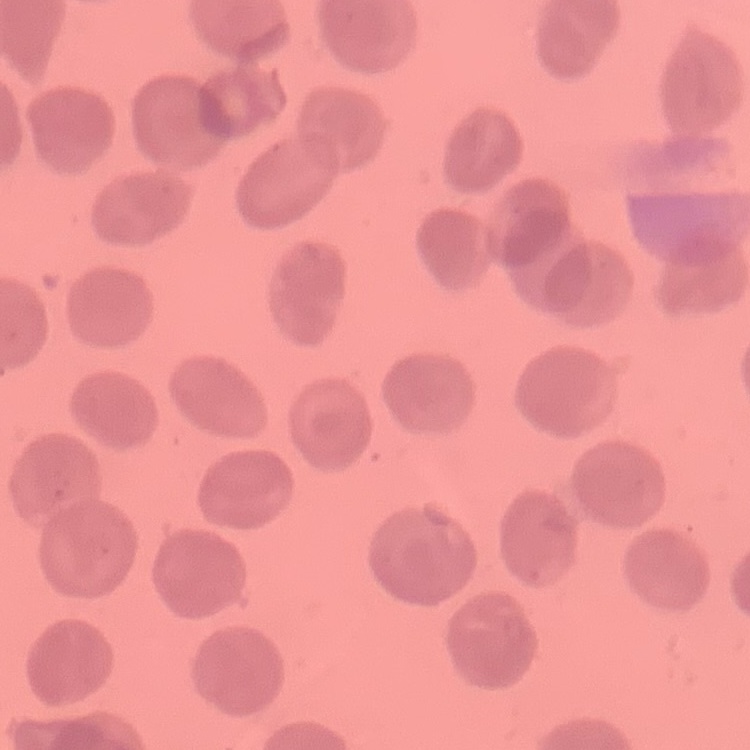
red blood cell morphology = no rouleaux formation
image type = one tile cut from a larger photomicrograph
preparation = thin blood smear
stain = Field's or Giemsa